Name the parasite shown.
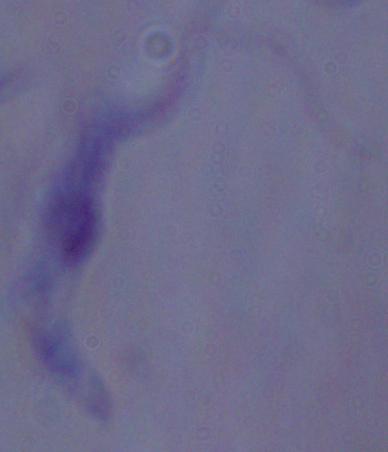

A trypanosome.

magnification = 1000x
modality = micrograph